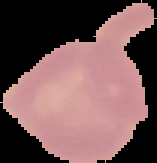

Summary:
  - Preparation: thin blood smear
  - Result: negative for Plasmodium parasites
  - Image size: 157×163 pixels
  - Image type: segmented cell region on a black background